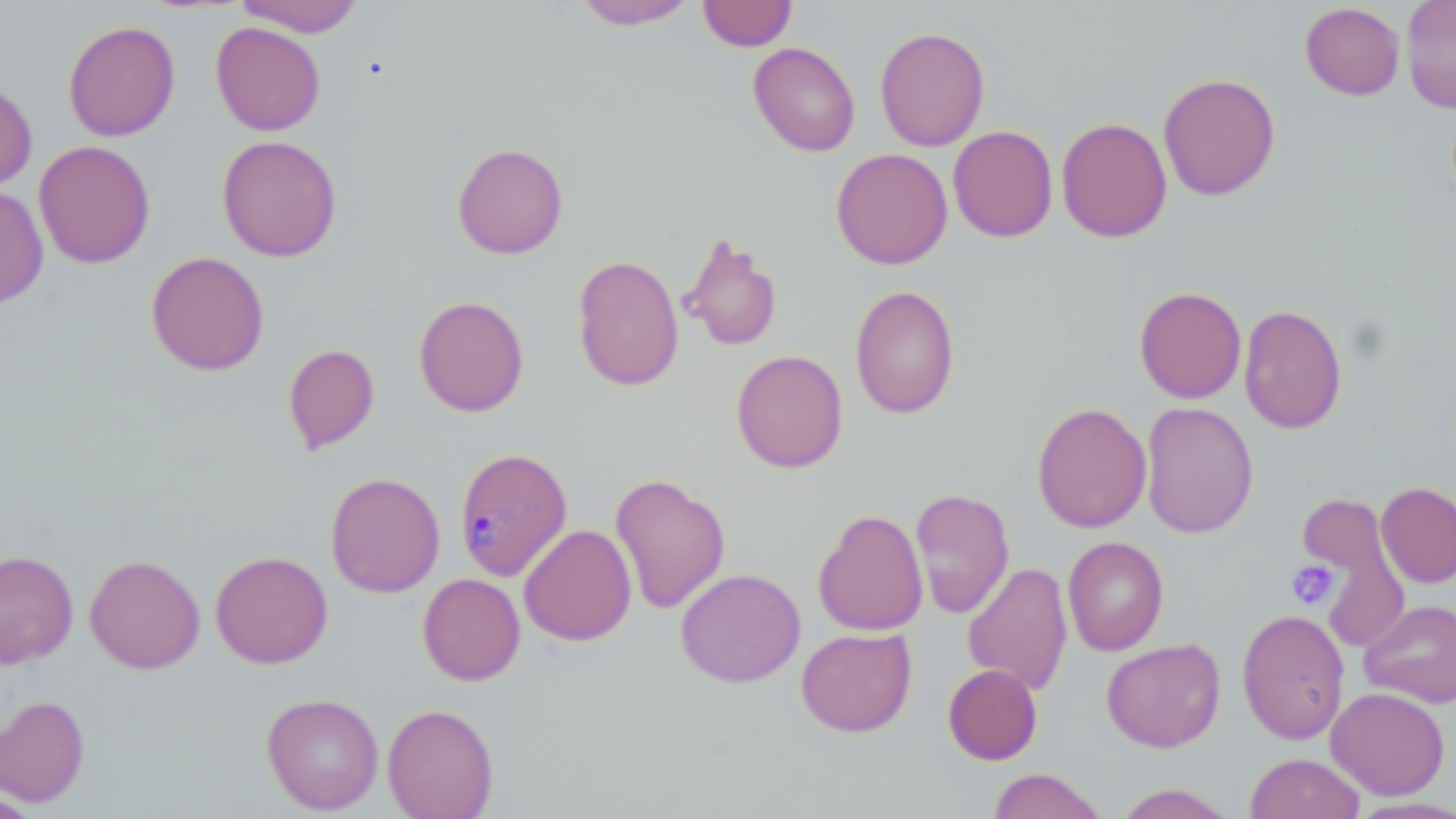
Approximate bounding boxes as (x1, y1, x2, y2) in pixels. Plasmodium malariae-infected red blood cell locations: (454, 447, 572, 581). Uninfected red blood cell locations: (234, 0, 364, 37), (698, 0, 797, 51), (1401, 0, 1456, 114), (573, 1, 698, 30), (1300, 2, 1405, 100), (62, 20, 181, 141), (210, 21, 326, 136), (875, 26, 990, 152), (748, 42, 860, 156), (1158, 72, 1281, 201), (0, 78, 37, 193), (1056, 117, 1172, 243), (948, 125, 1058, 243), (216, 134, 342, 262), (34, 140, 156, 269), (451, 142, 569, 259), (830, 148, 953, 270), (0, 186, 49, 310), (678, 232, 783, 352), (146, 251, 269, 376), (572, 254, 684, 392), (850, 284, 960, 420), (1134, 286, 1247, 404), (414, 295, 529, 417), (1239, 303, 1348, 434), (283, 343, 380, 453), (731, 349, 848, 473), (1140, 401, 1258, 539), (1031, 402, 1152, 533), (610, 471, 731, 615), (325, 472, 445, 598), (1376, 482, 1456, 588), (910, 487, 1015, 619), (1296, 492, 1407, 652), (812, 508, 929, 636), (519, 524, 637, 645), (1062, 536, 1168, 656), (0, 550, 78, 669), (210, 550, 333, 669), (84, 554, 205, 673), (963, 560, 1073, 696), (675, 568, 806, 688), (418, 573, 525, 685), (1359, 599, 1456, 707), (1237, 609, 1350, 744), (796, 627, 917, 737), (1101, 637, 1226, 753), (943, 663, 1042, 765), (1326, 686, 1450, 799), (261, 692, 384, 814), (0, 694, 90, 808), (382, 702, 499, 819), (1246, 753, 1366, 819), (986, 768, 1108, 819), (1114, 784, 1239, 819). Platelet locations: (1286, 560, 1339, 610). Slide-level diagnosis: Plasmodium malariae. Single field of view. Thin blood smear. Image is 1456×819 pixels. Captured at 1000x magnification. Light microscopy. May-Grünwald-Giemsa stain.